Describe the morphology of the erythrocytes.
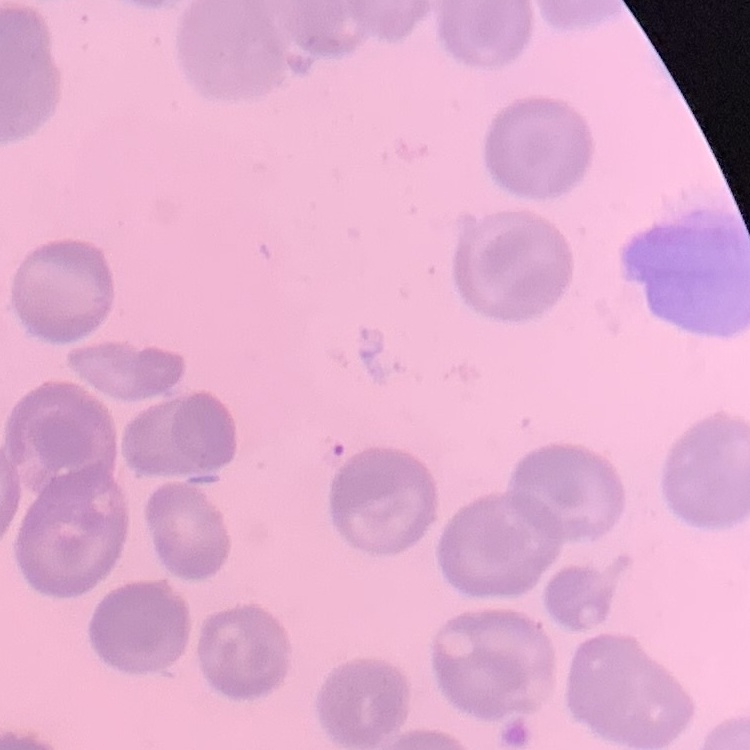

They show no rouleaux formation.

stain = Field's or Giemsa
preparation = thin blood smear
image type = one tile cut from a larger photomicrograph